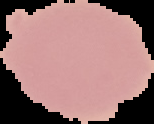

Summary:
  - Preparation: thin blood film
  - Image type: segmented cell region on a black background
  - Image size: 154×124 pixels
  - Malaria status: uninfected